Comment on the morphology of the red blood cells.
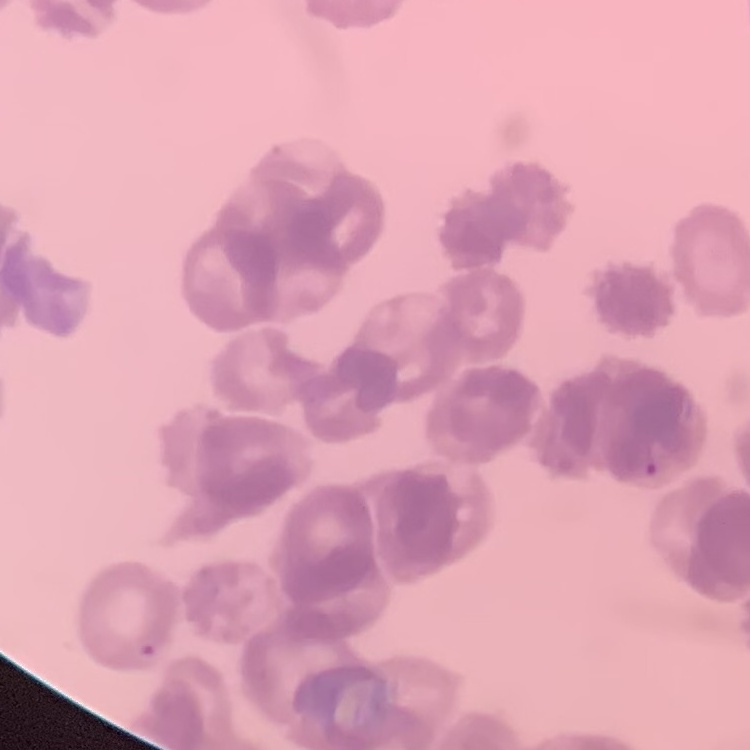
They show rouleaux formation.

Thin peripheral smear. Square crop of a larger photomicrograph. Stained with either Field's or Giemsa.